Name the cell type shown.
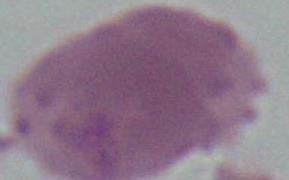

An erythrocyte.

Summary:
  - Modality: photomicrograph
  - Magnification: 1000x